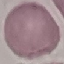
malaria status = uninfected
image type = cell patch, automatically extracted from a larger field of view and resized to 64 × 64 pixels
capture = smartphone camera at the microscope eyepiece
stain = Giemsa
preparation = thin blood smear